Identify the cell.
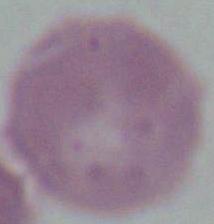
An erythrocyte.

magnification = 1000x
modality = micrograph